Locate every Plasmodium vivax-infected red blood cell.
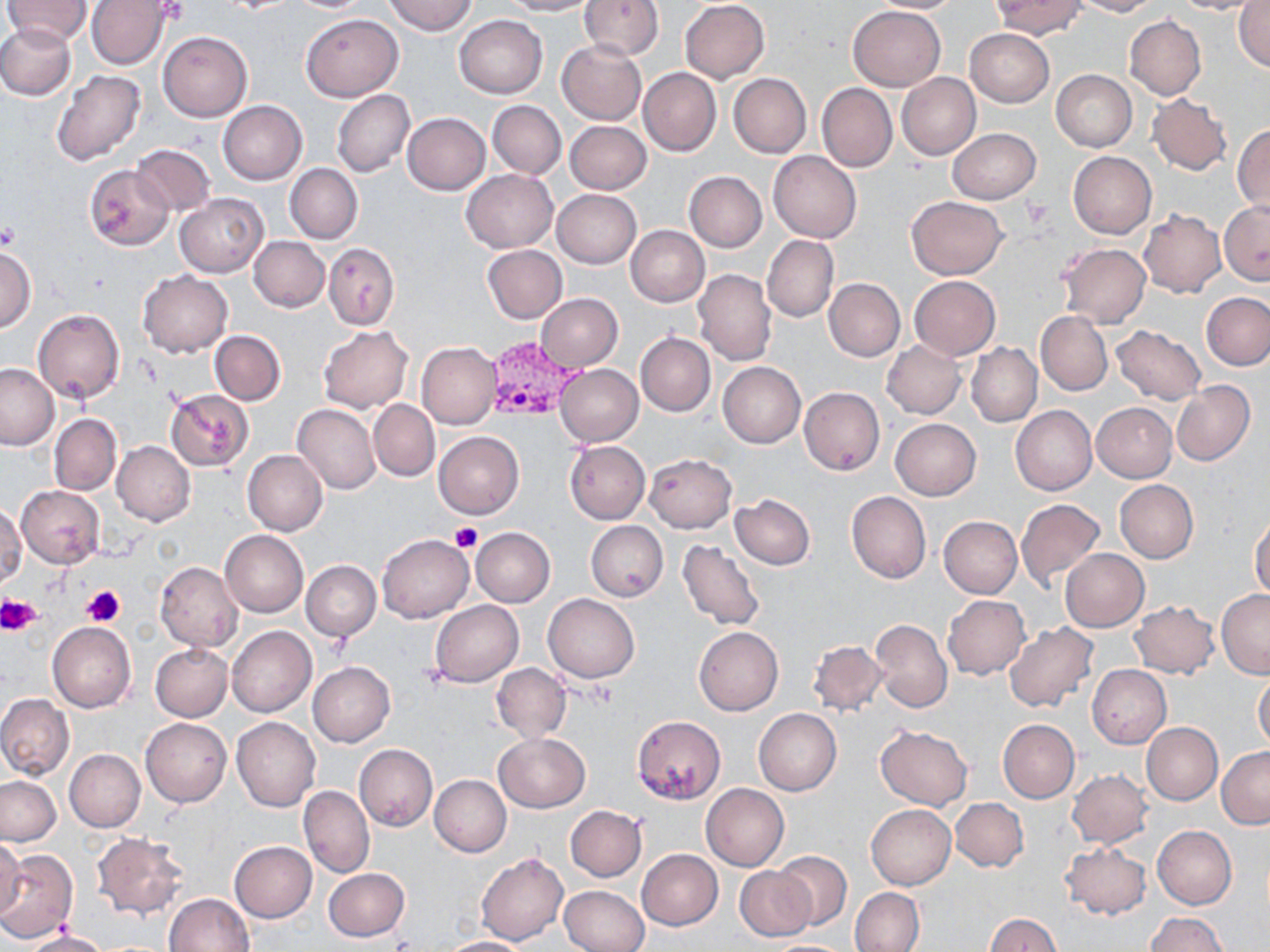

Approximate bounding boxes as named x1/y1/x2/y2 corners in pixels.
Plasmodium vivax-infected red blood cells: (x1=485, y1=336, x2=583, y2=421).

slide-level diagnosis = Plasmodium vivax
platelet locations = approximate bounding boxes as named x1/y1/x2/y2 corners in pixels: (x1=1022, y1=195, x2=1053, y2=226), (x1=0, y1=224, x2=20, y2=251), (x1=451, y1=521, x2=481, y2=553), (x1=81, y1=585, x2=126, y2=626), (x1=3, y1=595, x2=43, y2=634)
preparation = thin blood film
magnification = 1000x
image size = 1270×952 pixels
field of view = one of a larger specimen
stain = May-Grünwald-Giemsa
modality = light microscopy
uninfected red blood cell locations = approximate bounding boxes as named x1/y1/x2/y2 corners in pixels: (x1=2, y1=0, x2=92, y2=46), (x1=86, y1=0, x2=172, y2=69), (x1=383, y1=0, x2=477, y2=36), (x1=500, y1=0, x2=595, y2=16), (x1=868, y1=0, x2=963, y2=13), (x1=1071, y1=0, x2=1161, y2=16), (x1=1234, y1=0, x2=1270, y2=74), (x1=580, y1=1, x2=663, y2=61), (x1=680, y1=1, x2=770, y2=82), (x1=990, y1=1, x2=1085, y2=38), (x1=1170, y1=1, x2=1265, y2=15), (x1=848, y1=5, x2=946, y2=91), (x1=301, y1=14, x2=402, y2=102), (x1=455, y1=15, x2=548, y2=98), (x1=1124, y1=15, x2=1206, y2=101), (x1=0, y1=23, x2=75, y2=100), (x1=965, y1=28, x2=1055, y2=107), (x1=158, y1=31, x2=252, y2=121), (x1=556, y1=40, x2=646, y2=125), (x1=638, y1=67, x2=721, y2=156), (x1=1051, y1=69, x2=1137, y2=151), (x1=51, y1=70, x2=147, y2=166), (x1=728, y1=73, x2=811, y2=158), (x1=897, y1=73, x2=981, y2=159), (x1=816, y1=83, x2=896, y2=171), (x1=331, y1=89, x2=415, y2=178), (x1=1147, y1=93, x2=1232, y2=176), (x1=217, y1=100, x2=307, y2=185), (x1=336, y1=101, x2=492, y2=182), (x1=488, y1=101, x2=566, y2=178), (x1=403, y1=113, x2=491, y2=194), (x1=564, y1=120, x2=651, y2=194), (x1=1233, y1=124, x2=1270, y2=217), (x1=947, y1=128, x2=1041, y2=204), (x1=131, y1=143, x2=217, y2=217), (x1=768, y1=150, x2=861, y2=243), (x1=1068, y1=150, x2=1157, y2=239), (x1=285, y1=163, x2=363, y2=244), (x1=85, y1=165, x2=173, y2=250), (x1=461, y1=169, x2=557, y2=252), (x1=685, y1=171, x2=767, y2=252), (x1=552, y1=188, x2=642, y2=269), (x1=175, y1=193, x2=268, y2=277), (x1=906, y1=197, x2=1006, y2=279), (x1=1219, y1=200, x2=1270, y2=286), (x1=1139, y1=210, x2=1225, y2=297), (x1=626, y1=225, x2=709, y2=307), (x1=762, y1=234, x2=838, y2=322), (x1=250, y1=236, x2=330, y2=312), (x1=323, y1=243, x2=399, y2=331), (x1=1058, y1=243, x2=1152, y2=327), (x1=483, y1=245, x2=567, y2=323), (x1=0, y1=246, x2=36, y2=334), (x1=693, y1=269, x2=776, y2=367), (x1=137, y1=270, x2=233, y2=357), (x1=910, y1=276, x2=1000, y2=359), (x1=823, y1=278, x2=905, y2=362), (x1=1203, y1=292, x2=1270, y2=370), (x1=535, y1=293, x2=623, y2=371), (x1=545, y1=293, x2=630, y2=448), (x1=34, y1=308, x2=125, y2=405), (x1=1036, y1=311, x2=1112, y2=395), (x1=1111, y1=325, x2=1206, y2=406), (x1=318, y1=326, x2=413, y2=413), (x1=210, y1=330, x2=285, y2=405), (x1=635, y1=332, x2=715, y2=416), (x1=882, y1=339, x2=965, y2=418), (x1=416, y1=341, x2=501, y2=429), (x1=966, y1=343, x2=1042, y2=427), (x1=0, y1=362, x2=59, y2=450), (x1=718, y1=362, x2=806, y2=448), (x1=555, y1=364, x2=643, y2=446), (x1=1170, y1=379, x2=1254, y2=466), (x1=799, y1=387, x2=885, y2=475), (x1=165, y1=390, x2=255, y2=471), (x1=369, y1=400, x2=440, y2=481), (x1=1091, y1=401, x2=1176, y2=482), (x1=293, y1=403, x2=381, y2=494), (x1=1010, y1=405, x2=1097, y2=495), (x1=50, y1=414, x2=121, y2=495), (x1=890, y1=418, x2=981, y2=500), (x1=434, y1=430, x2=524, y2=518), (x1=564, y1=440, x2=650, y2=524), (x1=111, y1=441, x2=195, y2=525), (x1=235, y1=450, x2=319, y2=616), (x1=243, y1=450, x2=328, y2=534), (x1=645, y1=453, x2=736, y2=533), (x1=1115, y1=479, x2=1198, y2=563), (x1=16, y1=485, x2=104, y2=568), (x1=846, y1=491, x2=931, y2=583), (x1=731, y1=494, x2=815, y2=570), (x1=1015, y1=499, x2=1105, y2=589), (x1=1, y1=505, x2=25, y2=587), (x1=939, y1=516, x2=1021, y2=598), (x1=1250, y1=516, x2=1270, y2=598), (x1=585, y1=521, x2=667, y2=601), (x1=470, y1=527, x2=555, y2=607), (x1=220, y1=530, x2=308, y2=617), (x1=377, y1=534, x2=473, y2=622), (x1=678, y1=539, x2=765, y2=632), (x1=1060, y1=549, x2=1149, y2=632), (x1=301, y1=560, x2=381, y2=641), (x1=154, y1=562, x2=245, y2=653), (x1=1216, y1=589, x2=1270, y2=677), (x1=543, y1=594, x2=639, y2=683), (x1=943, y1=595, x2=1028, y2=680), (x1=430, y1=600, x2=522, y2=687), (x1=1130, y1=600, x2=1220, y2=678), (x1=870, y1=620, x2=953, y2=712), (x1=48, y1=621, x2=136, y2=712), (x1=1003, y1=622, x2=1099, y2=713), (x1=227, y1=626, x2=316, y2=717), (x1=694, y1=626, x2=784, y2=715), (x1=808, y1=639, x2=887, y2=718), (x1=151, y1=643, x2=232, y2=722), (x1=308, y1=661, x2=395, y2=747), (x1=491, y1=663, x2=571, y2=742), (x1=1087, y1=664, x2=1172, y2=748), (x1=1253, y1=671, x2=1270, y2=752), (x1=0, y1=693, x2=74, y2=781), (x1=754, y1=708, x2=841, y2=794), (x1=632, y1=716, x2=725, y2=804), (x1=232, y1=717, x2=321, y2=813), (x1=141, y1=718, x2=232, y2=806), (x1=997, y1=719, x2=1079, y2=803), (x1=1141, y1=722, x2=1223, y2=806), (x1=876, y1=724, x2=972, y2=810), (x1=494, y1=732, x2=590, y2=813), (x1=354, y1=744, x2=437, y2=831), (x1=1217, y1=746, x2=1270, y2=830), (x1=65, y1=749, x2=145, y2=831), (x1=1067, y1=769, x2=1151, y2=848), (x1=430, y1=775, x2=511, y2=856), (x1=0, y1=776, x2=61, y2=846), (x1=701, y1=783, x2=789, y2=871), (x1=299, y1=785, x2=375, y2=878), (x1=950, y1=797, x2=1028, y2=872), (x1=866, y1=803, x2=955, y2=889), (x1=565, y1=805, x2=647, y2=881), (x1=1153, y1=826, x2=1237, y2=909), (x1=91, y1=833, x2=190, y2=918), (x1=0, y1=836, x2=26, y2=919), (x1=229, y1=841, x2=317, y2=923), (x1=1060, y1=842, x2=1152, y2=921), (x1=0, y1=849, x2=78, y2=942), (x1=637, y1=849, x2=722, y2=930), (x1=774, y1=851, x2=853, y2=929), (x1=476, y1=852, x2=568, y2=946), (x1=562, y1=865, x2=720, y2=941), (x1=734, y1=865, x2=815, y2=942), (x1=322, y1=867, x2=410, y2=942), (x1=560, y1=884, x2=650, y2=952), (x1=850, y1=887, x2=925, y2=951), (x1=165, y1=892, x2=254, y2=952), (x1=985, y1=912, x2=1061, y2=952), (x1=1146, y1=912, x2=1227, y2=952), (x1=24, y1=928, x2=109, y2=952), (x1=436, y1=937, x2=531, y2=952), (x1=762, y1=939, x2=854, y2=951)